Assess for Plasmodium parasites.
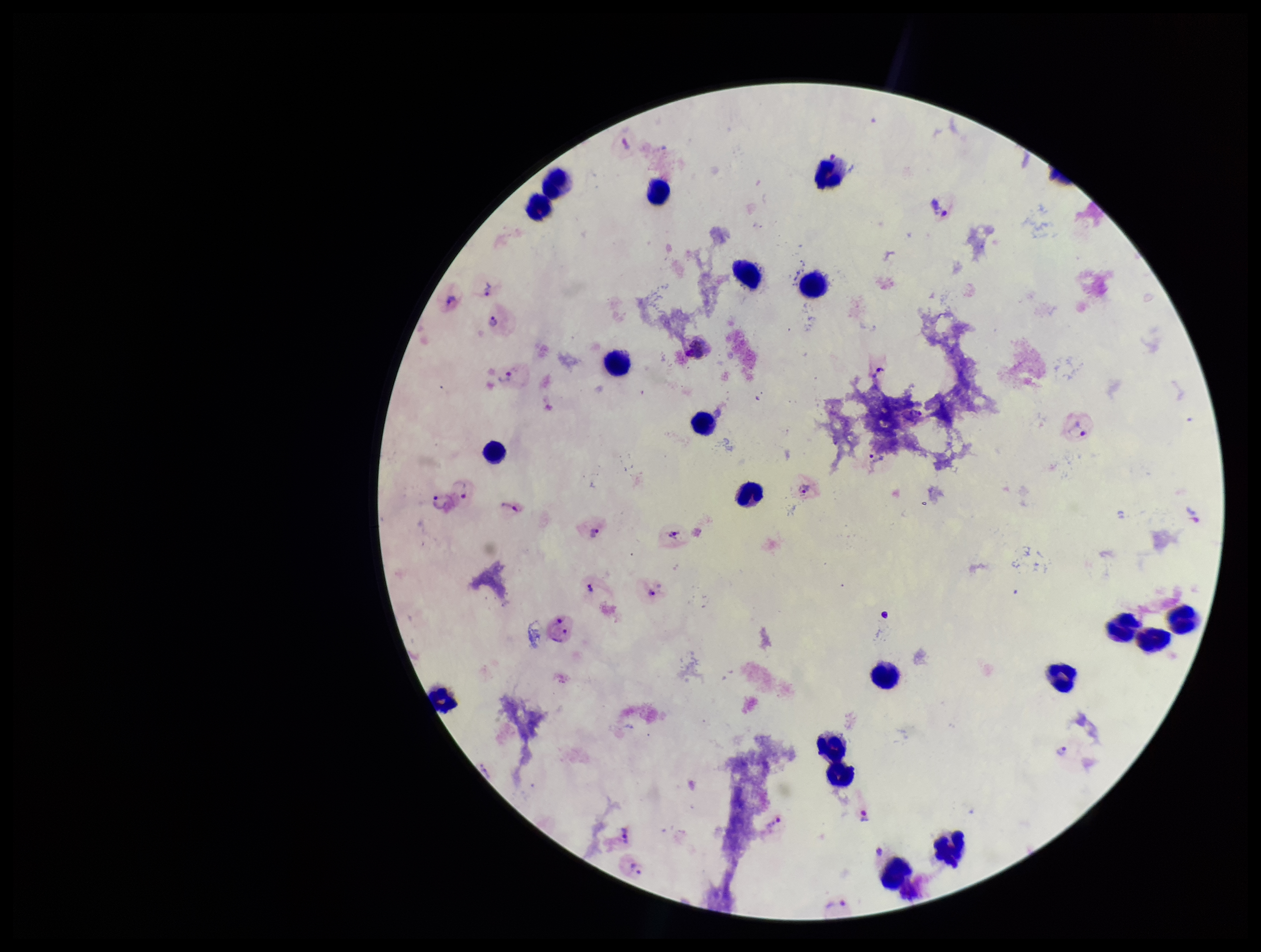

Detected.

Summary:
  - Patient malaria status: positive
  - Stain: Giemsa
  - Image size: 1261×952 pixels
  - Parasite count: 18
  - Species reported for this patient: Plasmodium vivax
  - Leukocyte count: 20
  - Preparation: thick blood smear
  - Field of view: one from this slide
  - Capture: smartphone photograph through the microscope eyepiece